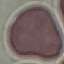

malaria status = uninfected
capture = smartphone through the microscope eyepiece
preparation = thin blood film
image type = automatically extracted cell patch, resized to 64 × 64 pixels
stain = Giemsa